Name the cell type shown.
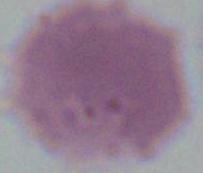

An erythrocyte.

Micrograph. 1000x magnification.